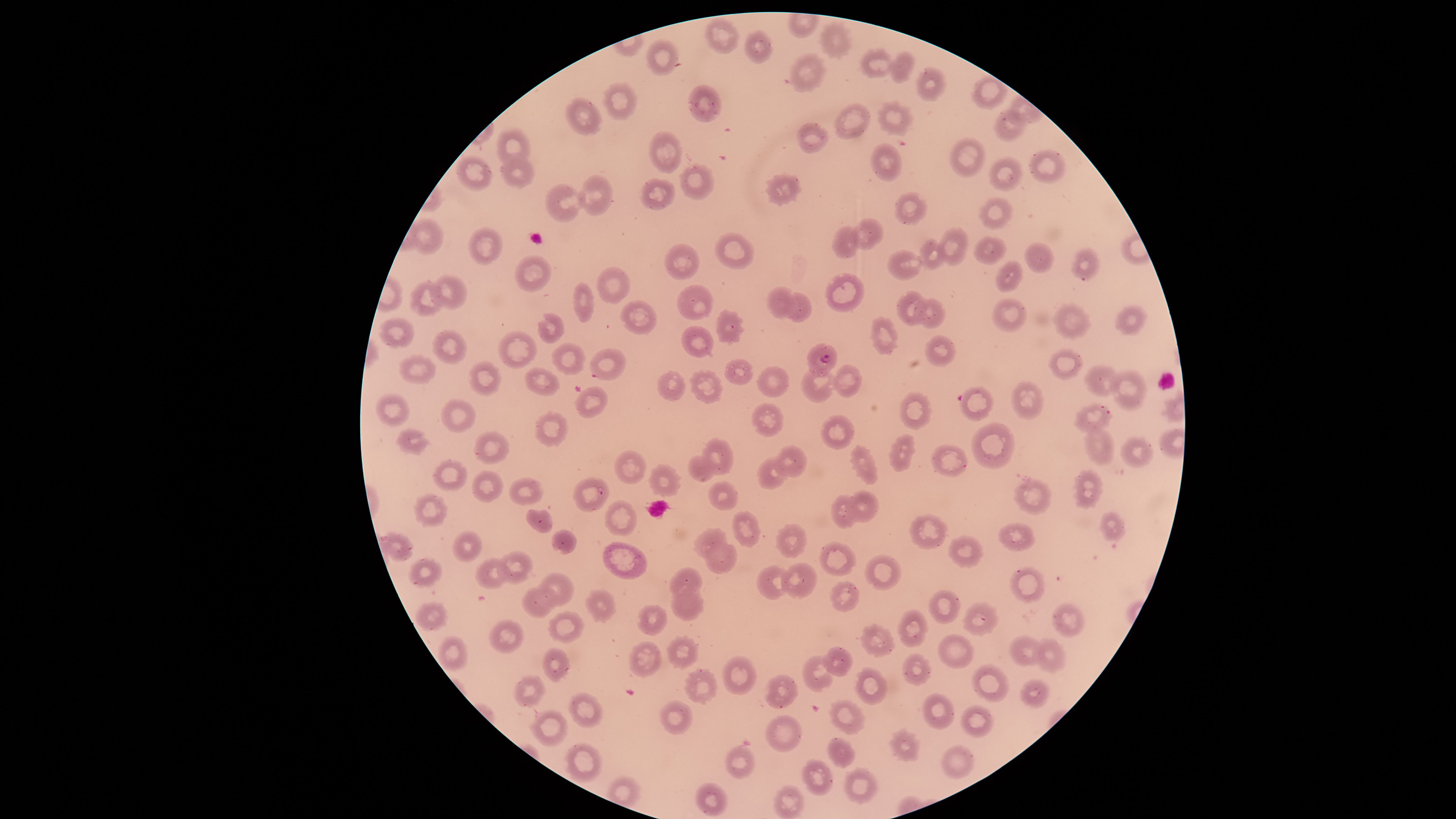

parasitized_red_blood_cells: 'approximate bounding boxes as (left, top, right, bottom) in pixels: (806, 343, 838, 377)'
presence: malaria parasites seen
uninfected_red_blood_cells: 'approximate bounding boxes as (left, top, right, bottom) in pixels: (705, 18, 740, 53), (822, 24, 851, 58), (746, 30, 774, 63), (647, 40, 678, 76), (861, 48, 894, 77), (889, 51, 915, 82), (791, 53, 825, 92), (916, 67, 947, 102), (604, 84, 635, 120), (688, 85, 722, 123), (565, 98, 603, 137), (877, 101, 911, 136), (834, 102, 872, 140), (995, 109, 1028, 141), (797, 122, 829, 153), (495, 127, 531, 168), (649, 130, 681, 174), (950, 137, 986, 177), (871, 144, 902, 182), (1029, 149, 1067, 184), (500, 153, 535, 189), (456, 157, 492, 190), (989, 158, 1023, 191), (680, 164, 714, 200), (579, 174, 614, 215), (765, 175, 801, 205), (640, 178, 675, 210), (545, 184, 585, 222), (892, 192, 928, 225), (978, 197, 1014, 231), (851, 218, 886, 249), (408, 219, 443, 254), (832, 225, 860, 259), (936, 226, 968, 265), (469, 227, 503, 265), (714, 232, 754, 270), (974, 236, 1007, 264), (917, 238, 947, 269), (1025, 241, 1056, 273), (665, 244, 699, 280), (1071, 247, 1098, 280), (886, 248, 923, 281), (514, 254, 551, 292), (996, 261, 1023, 291), (595, 266, 630, 304), (826, 273, 865, 312), (430, 276, 468, 309), (410, 282, 445, 317), (573, 282, 594, 322), (676, 284, 714, 321), (766, 286, 798, 319), (896, 291, 929, 326), (784, 292, 812, 323), (994, 297, 1027, 331), (915, 298, 946, 328), (619, 299, 658, 334), (1054, 303, 1092, 339), (1116, 305, 1148, 335), (715, 309, 742, 344), (538, 314, 564, 345), (378, 317, 415, 348), (870, 318, 899, 355), (681, 326, 714, 358), (431, 329, 467, 364), (498, 330, 537, 369), (925, 334, 956, 366), (552, 343, 585, 376), (590, 348, 626, 381), (1049, 348, 1084, 380), (397, 354, 437, 383), (725, 357, 754, 385), (468, 361, 502, 396), (800, 364, 835, 403), (831, 364, 861, 397), (523, 366, 559, 396), (756, 366, 790, 398), (1083, 366, 1119, 396), (656, 370, 686, 401), (689, 370, 723, 403), (1111, 370, 1146, 410), (1010, 381, 1044, 420), (575, 385, 607, 418), (959, 386, 994, 421), (900, 392, 931, 430), (376, 393, 409, 427), (441, 398, 475, 432), (751, 402, 783, 438), (1074, 404, 1111, 432), (535, 411, 567, 445), (819, 414, 854, 450), (970, 423, 1015, 469), (1083, 426, 1115, 465), (397, 428, 427, 454), (474, 431, 508, 464), (889, 433, 914, 470), (702, 437, 734, 475), (1120, 437, 1153, 468), (852, 445, 877, 483), (931, 445, 968, 476), (775, 446, 806, 477), (613, 450, 647, 485), (686, 455, 718, 482), (756, 456, 788, 491), (433, 459, 467, 492), (649, 464, 681, 498), (472, 470, 503, 502), (1075, 471, 1102, 508), (572, 477, 610, 513), (509, 478, 543, 506), (1014, 480, 1053, 514), (708, 481, 737, 511), (846, 491, 879, 522), (414, 494, 448, 527), (830, 494, 859, 528), (604, 499, 637, 539), (526, 508, 554, 533), (733, 511, 759, 547), (1100, 512, 1126, 541), (910, 514, 948, 549), (999, 522, 1034, 550), (777, 524, 806, 556), (692, 528, 726, 559), (552, 529, 576, 554), (453, 530, 482, 562), (384, 532, 413, 561), (949, 535, 983, 567), (703, 538, 738, 573), (820, 541, 857, 576), (602, 542, 647, 580), (497, 552, 534, 583), (865, 555, 902, 590), (475, 557, 510, 588), (407, 558, 443, 587), (782, 563, 818, 598), (756, 565, 792, 600), (670, 566, 703, 598), (1010, 567, 1046, 603), (539, 573, 576, 608), (830, 580, 861, 612), (521, 585, 559, 619), (670, 586, 705, 621), (588, 589, 615, 621), (928, 590, 962, 623), (415, 601, 447, 633), (963, 602, 999, 635), (1050, 602, 1086, 637), (637, 605, 667, 635), (898, 609, 929, 648), (548, 612, 584, 644), (489, 619, 524, 654), (862, 624, 894, 656), (938, 634, 975, 669), (1009, 635, 1046, 666), (438, 636, 467, 670), (666, 636, 699, 669), (1032, 639, 1067, 673), (628, 642, 662, 679), (542, 647, 570, 681), (824, 647, 854, 676), (903, 653, 932, 686), (723, 655, 757, 695), (802, 655, 834, 692), (973, 664, 1010, 702), (854, 667, 887, 705), (685, 670, 717, 703), (764, 674, 797, 710), (515, 675, 545, 706), (1019, 679, 1049, 708), (569, 692, 604, 728), (923, 693, 954, 730), (659, 699, 692, 735), (831, 700, 865, 734), (962, 704, 995, 737), (531, 711, 568, 746), (765, 715, 801, 753), (891, 729, 921, 761), (828, 738, 854, 768), (567, 743, 603, 782), (726, 745, 755, 779), (942, 745, 974, 779), (802, 760, 834, 796), (844, 768, 877, 803), (696, 782, 729, 815), (773, 785, 804, 818)'
image_size: 1456×819 pixels
field_of_view: single
capture: smartphone photograph through the microscope eyepiece
visible_region: circular
stain: Giemsa
species: Plasmodium falciparum
preparation: thin smear of blood